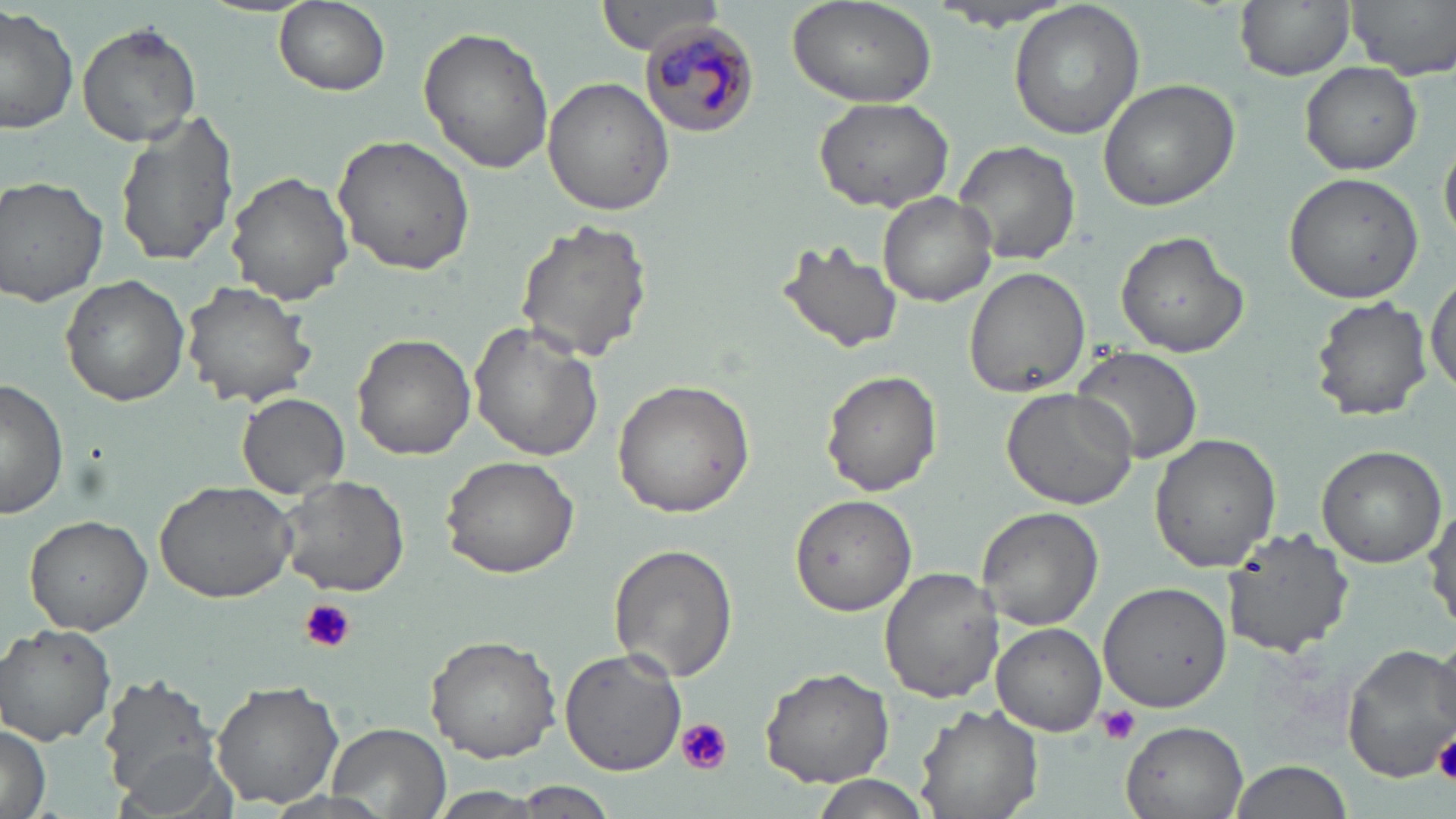
Approximate bounding boxes as (x1,y1)-(x2,y2) corner pairs in pixels. Uninfected red blood cell locations: (595,0)-(724,56), (929,0)-(1080,30), (1233,0)-(1357,81), (1347,0)-(1456,80), (273,1)-(391,97), (1007,1)-(1145,141), (786,2)-(937,112), (0,6)-(78,138), (77,21)-(203,147), (418,23)-(555,177), (1301,62)-(1422,174), (543,76)-(674,217), (1096,77)-(1244,212), (810,94)-(959,214), (114,107)-(241,272), (332,134)-(477,276), (953,139)-(1081,266), (226,171)-(353,305), (1282,171)-(1425,302), (0,175)-(110,307), (878,192)-(995,308), (514,217)-(654,365), (1115,229)-(1250,359), (772,239)-(904,357), (1426,263)-(1455,398), (962,267)-(1091,398), (61,276)-(190,407), (181,280)-(317,409), (1310,294)-(1433,422), (469,323)-(604,462), (351,333)-(478,460), (1070,346)-(1204,462), (821,369)-(944,497), (0,378)-(70,521), (611,381)-(757,518), (1000,387)-(1138,509), (236,393)-(349,497), (1149,432)-(1281,573), (1317,445)-(1447,567), (438,454)-(581,580), (276,473)-(411,598), (154,479)-(298,606), (790,495)-(917,616), (1427,499)-(1456,631), (975,505)-(1104,630), (24,514)-(151,634), (1220,528)-(1356,658), (608,542)-(739,684), (879,568)-(1003,703), (1101,581)-(1234,714), (992,621)-(1106,735), (2,624)-(118,745), (424,634)-(563,763), (1341,642)-(1456,780), (559,648)-(687,775), (761,666)-(894,787), (99,674)-(226,809), (211,683)-(344,808), (916,703)-(1042,819), (0,719)-(52,819), (1122,722)-(1248,818), (328,724)-(451,817), (111,744)-(238,819), (1225,759)-(1352,819), (808,777)-(933,819), (512,781)-(618,817), (424,787)-(555,817). Plasmodium malariae-infected red blood cell locations: (638,20)-(761,140). Platelet locations: (299,598)-(356,653), (1098,703)-(1141,745), (676,718)-(732,776), (1434,730)-(1456,786). Slide-level diagnosis: Plasmodium malariae. Thin blood film. May-Grünwald-Giemsa-stained preparation. Light microscopy. Image is 1456×819 pixels. One field of a larger specimen. Captured at 1000x magnification.